Assess this cell for malaria.
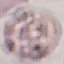

It is uninfected.

preparation = thin smear
image type = cell patch, automatically extracted from a larger field of view and resized to 64 × 64 pixels
stain = Giemsa
capture = smartphone camera at the microscope eyepiece